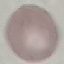

Result: no malaria parasites detected. Cell patch, automatically extracted from a larger field of view and resized to 64 × 64 pixels. Thin smear of blood. Acquired by smartphone through the microscope eyepiece. Giemsa-stained preparation.